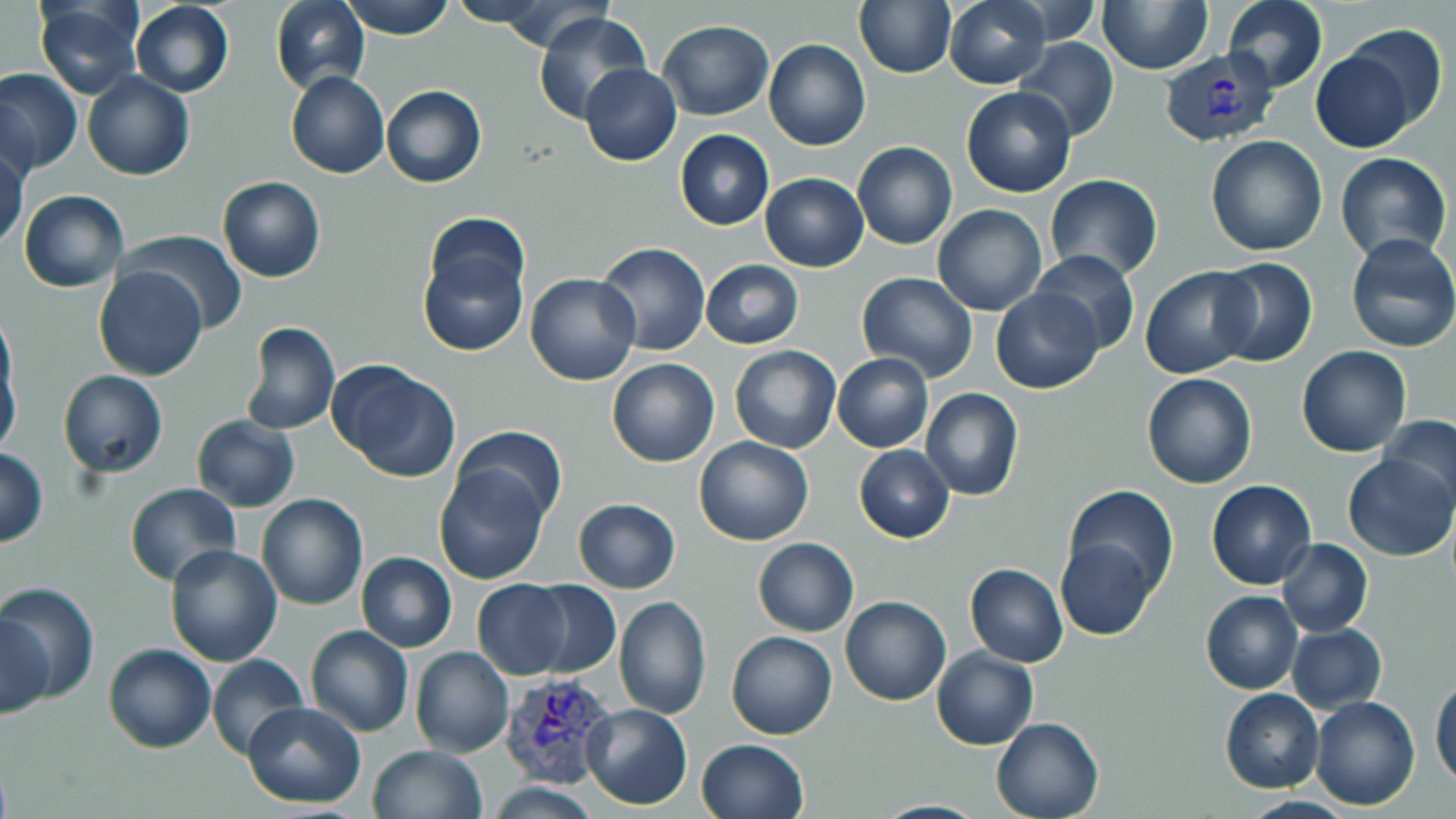

Approximate bounding boxes as (x1, y1, x2, y2) in pixels. Uninfected red blood cell locations: (270, 0, 370, 96), (340, 0, 455, 39), (446, 0, 557, 29), (494, 0, 617, 54), (1220, 0, 1328, 93), (33, 1, 144, 98), (854, 1, 956, 79), (945, 1, 1050, 88), (1005, 1, 1102, 45), (1099, 1, 1211, 74), (131, 2, 233, 97), (533, 11, 651, 126), (658, 20, 773, 120), (1337, 25, 1449, 133), (1014, 37, 1120, 142), (763, 39, 870, 151), (1311, 46, 1419, 151), (579, 64, 682, 166), (1, 69, 82, 174), (285, 71, 389, 179), (83, 72, 195, 180), (381, 85, 486, 188), (961, 85, 1076, 197), (675, 130, 773, 229), (1206, 136, 1328, 257), (852, 142, 958, 250), (0, 147, 27, 253), (1334, 152, 1453, 264), (763, 159, 957, 260), (759, 173, 868, 272), (1043, 173, 1164, 280), (217, 175, 325, 282), (19, 189, 128, 292), (933, 204, 1047, 315), (420, 215, 530, 343), (121, 230, 248, 336), (1346, 233, 1456, 353), (595, 241, 712, 356), (1030, 251, 1140, 355), (1209, 257, 1317, 367), (699, 259, 804, 348), (95, 265, 207, 381), (1140, 266, 1258, 379), (856, 273, 978, 381), (525, 274, 640, 387), (991, 287, 1105, 394), (240, 321, 340, 435), (0, 340, 20, 455), (1296, 345, 1412, 457), (730, 346, 841, 454), (832, 354, 933, 452), (607, 358, 720, 468), (326, 360, 462, 484), (58, 370, 167, 478), (1142, 373, 1256, 489), (920, 387, 1024, 501), (190, 414, 300, 512), (1378, 415, 1456, 516), (452, 425, 568, 527), (693, 435, 814, 546), (854, 445, 954, 543), (0, 449, 48, 546), (1342, 452, 1454, 561), (434, 464, 552, 584), (1206, 480, 1314, 589), (125, 482, 240, 585), (1066, 485, 1178, 597), (256, 494, 368, 611), (574, 498, 680, 593), (753, 537, 858, 637), (1054, 537, 1156, 640), (1277, 538, 1373, 638), (166, 545, 283, 665), (355, 551, 457, 652), (964, 562, 1068, 668), (471, 579, 573, 679), (0, 580, 100, 704), (524, 580, 621, 678), (1201, 591, 1303, 694), (614, 595, 712, 719), (840, 596, 951, 706), (1, 613, 51, 719), (1286, 624, 1387, 713), (306, 626, 414, 737), (262, 630, 402, 787), (727, 630, 837, 741), (102, 642, 216, 753), (409, 646, 514, 758), (932, 647, 1039, 749), (206, 652, 311, 762), (1430, 673, 1455, 787), (1220, 688, 1325, 793), (1310, 694, 1421, 811), (241, 701, 366, 807), (582, 703, 693, 810), (991, 716, 1105, 819), (696, 738, 808, 819), (368, 745, 487, 819), (488, 780, 599, 818). Plasmodium vivax-infected red blood cell locations: (1158, 48, 1278, 146), (498, 672, 619, 790). Slide-level diagnosis: Plasmodium vivax. 1000x magnification. Optical microscopy. One field of a larger specimen. Thin blood smear. Image is 1456×819 pixels. May-Grünwald-Giemsa-stained preparation.